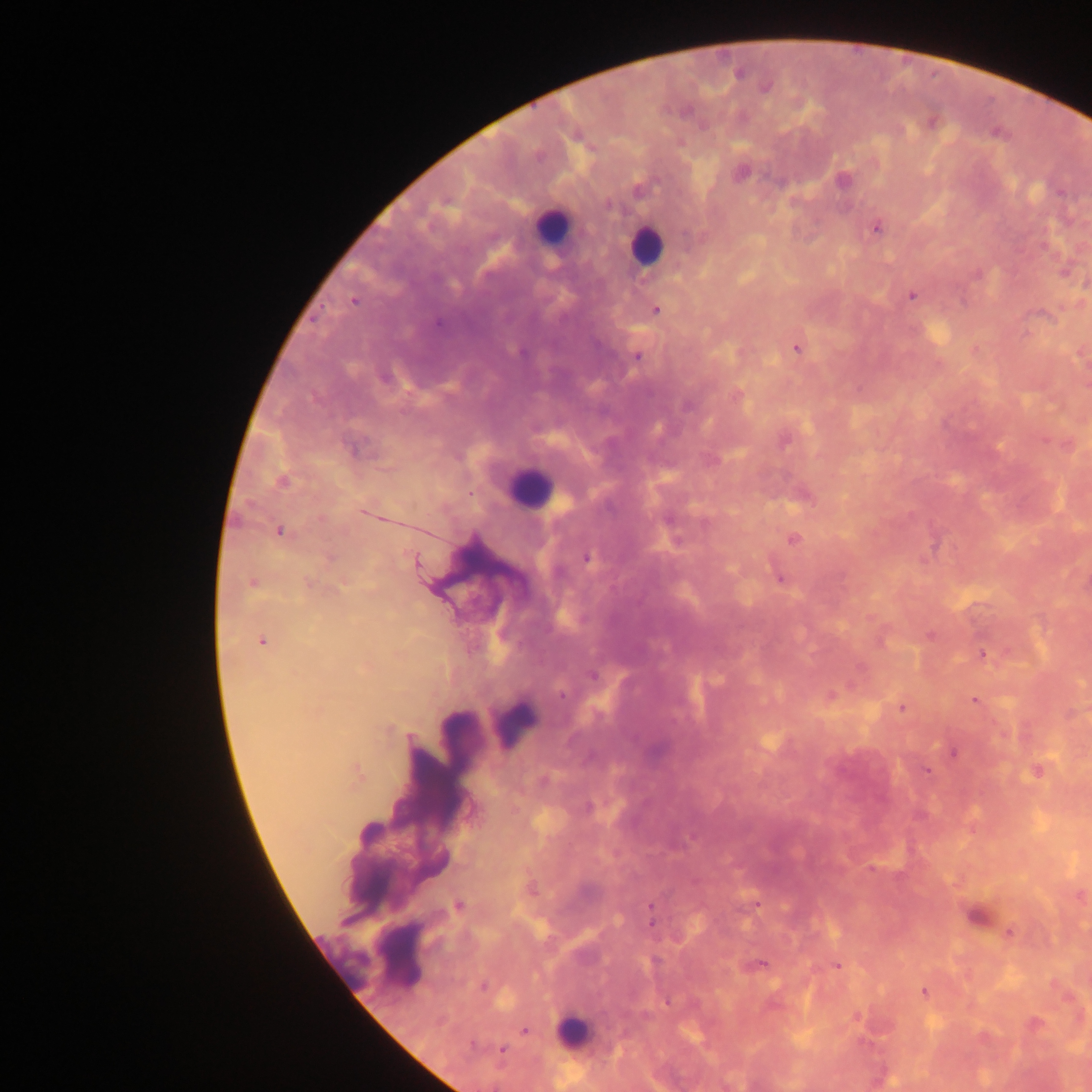
Approximate centers as [x, y] in pixels.
Summary:
  - Plasmodium parasite locations: [738, 73], [765, 87], [930, 122], [741, 172], [843, 180], [876, 227], [1065, 271], [978, 275], [912, 294], [354, 300], [656, 309], [796, 348], [636, 356], [736, 394], [1067, 445], [282, 481], [802, 494], [279, 531], [793, 539], [587, 557], [416, 561], [779, 577], [253, 583], [308, 583], [262, 641], [982, 654], [594, 675], [830, 696], [974, 700], [901, 707], [952, 751], [1036, 771], [357, 773], [588, 807], [1079, 895], [458, 905], [752, 906], [651, 910], [976, 916], [1009, 932], [757, 964], [836, 965], [924, 992], [1034, 1024], [525, 1031], [501, 1049]
  - Leukocyte locations: [551, 226], [645, 245], [528, 488], [514, 724], [399, 956], [571, 1032]
  - Preparation: thick blood smear
  - Field of view: single
  - Image size: 1092×1092 pixels
  - Capture: mobile-phone photograph through a microscope
  - Country: Ghana